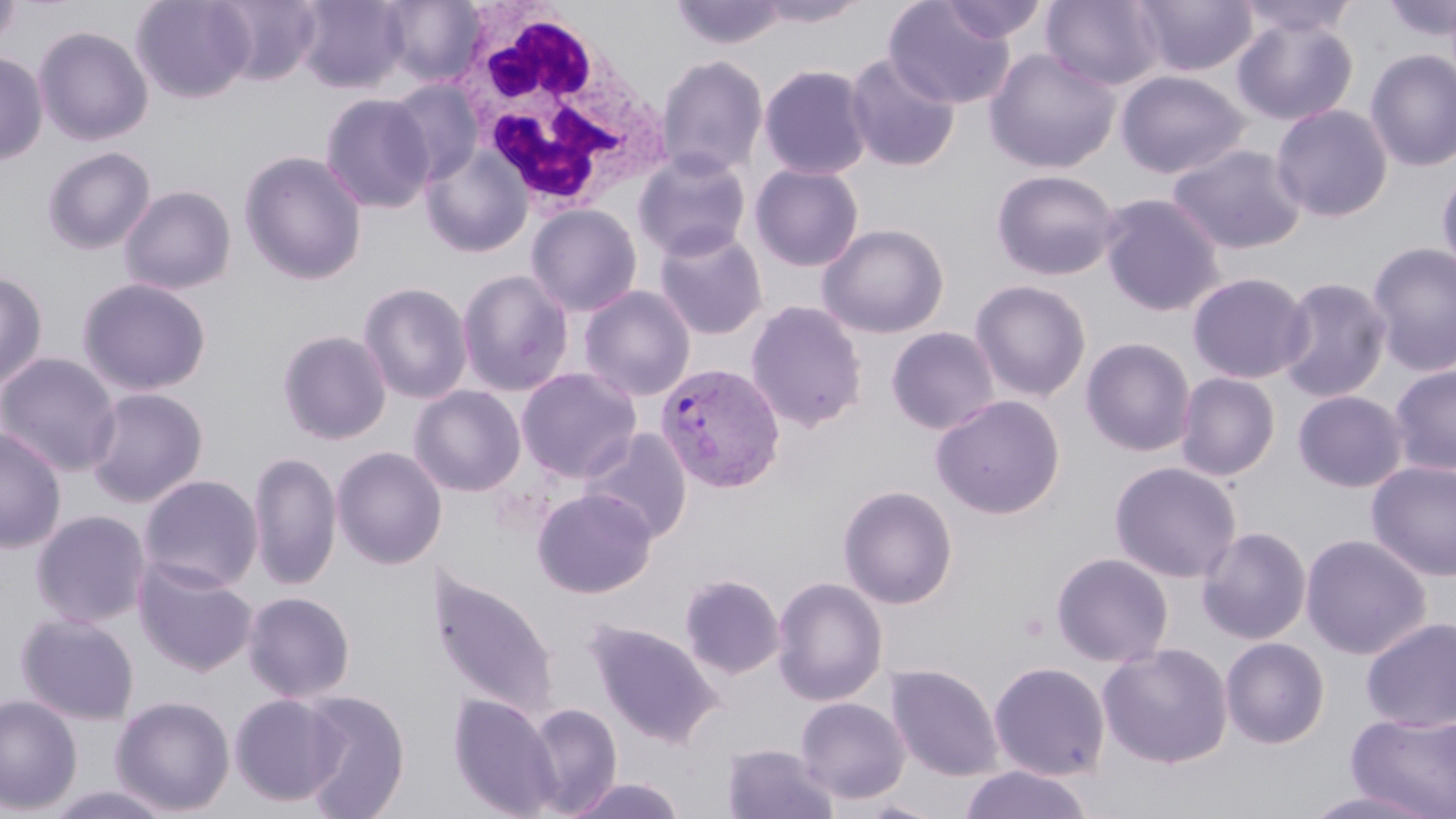
slide-level diagnosis = Plasmodium vivax
preparation = thin blood smear
modality = optical microscopy
Plasmodium vivax-infected red blood cell locations = approximate bounding boxes as (x1, y1, x2, y2) in pixels: (654, 362, 786, 494)
magnification = 1000x
image size = 1456×819 pixels
stain = May-Grünwald-Giemsa
uninfected red blood cell locations = approximate bounding boxes as (x1, y1, x2, y2) in pixels: (130, 0, 255, 103), (212, 0, 323, 86), (295, 0, 409, 94), (379, 0, 487, 86), (752, 0, 870, 28), (1040, 0, 1166, 90), (1132, 0, 1258, 77), (1234, 0, 1360, 40), (1379, 0, 1456, 44), (0, 1, 22, 52), (670, 1, 789, 52), (883, 1, 1016, 108), (937, 1, 1049, 45), (1231, 14, 1358, 126), (34, 25, 153, 147), (984, 48, 1121, 174), (1364, 49, 1456, 172), (0, 51, 48, 165), (844, 53, 961, 172), (656, 54, 769, 178), (757, 64, 874, 180), (1115, 69, 1250, 180), (384, 79, 485, 185), (320, 92, 435, 214), (1270, 103, 1394, 223), (1166, 143, 1307, 254), (420, 145, 533, 258), (41, 146, 156, 255), (632, 149, 753, 262), (239, 150, 368, 286), (749, 163, 865, 272), (991, 169, 1121, 281), (1437, 169, 1456, 278), (118, 185, 237, 295), (1097, 193, 1226, 317), (525, 203, 643, 317), (817, 222, 949, 339), (652, 226, 768, 341), (1366, 241, 1456, 377), (456, 268, 575, 397), (0, 270, 49, 390), (1187, 271, 1312, 384), (1275, 275, 1392, 403), (76, 277, 213, 397), (970, 279, 1092, 402), (357, 281, 473, 404), (578, 285, 696, 401), (745, 299, 868, 433), (886, 326, 1000, 436), (276, 329, 392, 445), (1081, 337, 1196, 457), (0, 352, 121, 477), (1389, 363, 1456, 476), (516, 367, 641, 483), (1175, 372, 1280, 481), (409, 385, 527, 497), (84, 387, 208, 507), (1292, 389, 1409, 492), (930, 394, 1066, 519), (0, 427, 66, 553), (580, 427, 693, 544), (331, 446, 447, 570), (248, 449, 341, 590), (1109, 460, 1242, 583), (1365, 460, 1456, 581), (138, 474, 263, 593), (838, 484, 958, 610), (532, 487, 657, 598), (30, 509, 151, 628), (1197, 526, 1312, 645), (1299, 533, 1432, 659), (1051, 551, 1174, 668), (133, 558, 257, 676), (429, 568, 561, 724), (679, 574, 785, 679), (772, 575, 888, 707), (243, 590, 356, 702), (15, 612, 140, 725), (1360, 616, 1456, 733), (587, 620, 722, 747), (1220, 637, 1330, 748), (1097, 642, 1234, 768), (989, 661, 1110, 781), (886, 663, 1003, 781), (298, 690, 410, 818), (229, 693, 346, 807), (448, 693, 562, 818), (0, 694, 82, 815), (111, 695, 235, 816), (795, 696, 911, 804), (523, 702, 623, 816), (1345, 710, 1456, 819), (722, 743, 838, 819), (959, 765, 1093, 819), (565, 777, 689, 819), (43, 785, 178, 819), (1297, 786, 1447, 819)
field of view = single
white blood cell locations = approximate bounding boxes as (x1, y1, x2, y2) in pixels: (449, 9, 666, 212)